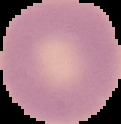
Malaria status: uninfected. The area outside the segmented cell region is set to black. Image is 121×124 pixels. From a thin blood film.